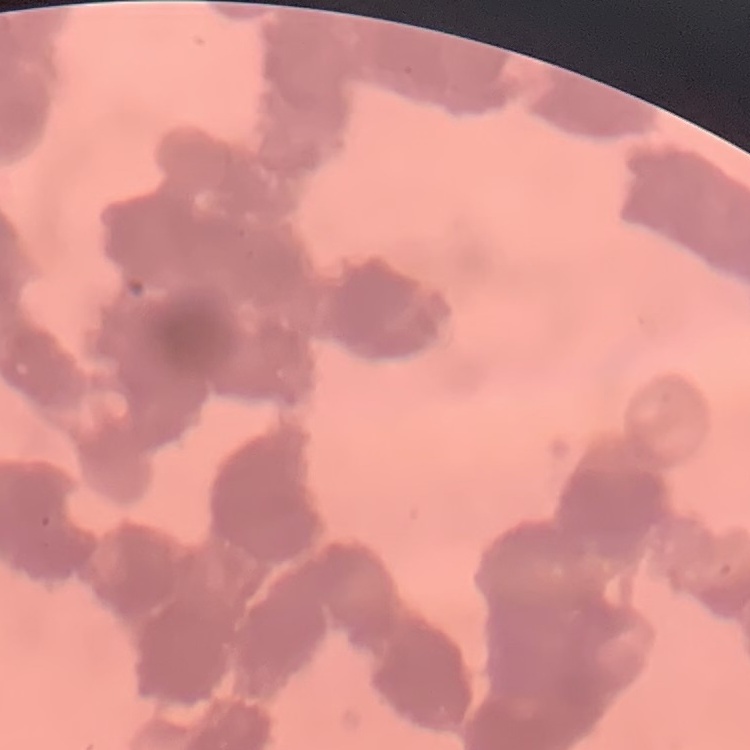

Summary:
  - Red blood cell morphology: rouleaux formation
  - Image type: one tile cut from a larger photomicrograph
  - Stain: Field's or Giemsa
  - Preparation: thin blood smear